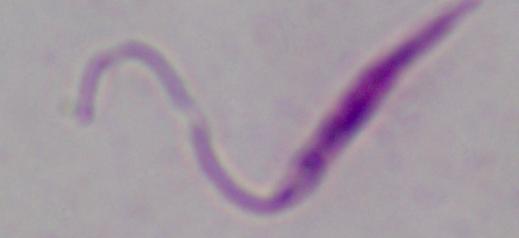
A Leishmania parasite is seen. Photomicrograph. 1000x magnification.